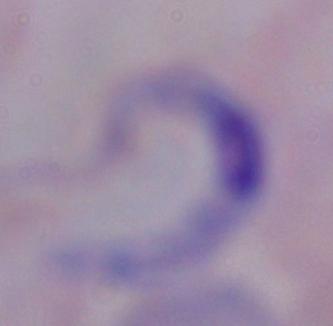
modality = photomicrograph
identification = trypanosome
magnification = 1000x